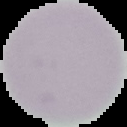

Result: negative for malaria parasites. Image is 127×127 pixels. From a thin blood smear. Segmented cell region on a black background.